Report the malaria status of this cell.
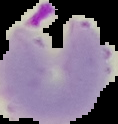

It is parasitized.

image type = segmented cell region on a black background
preparation = thin blood film
image size = 118×124 pixels